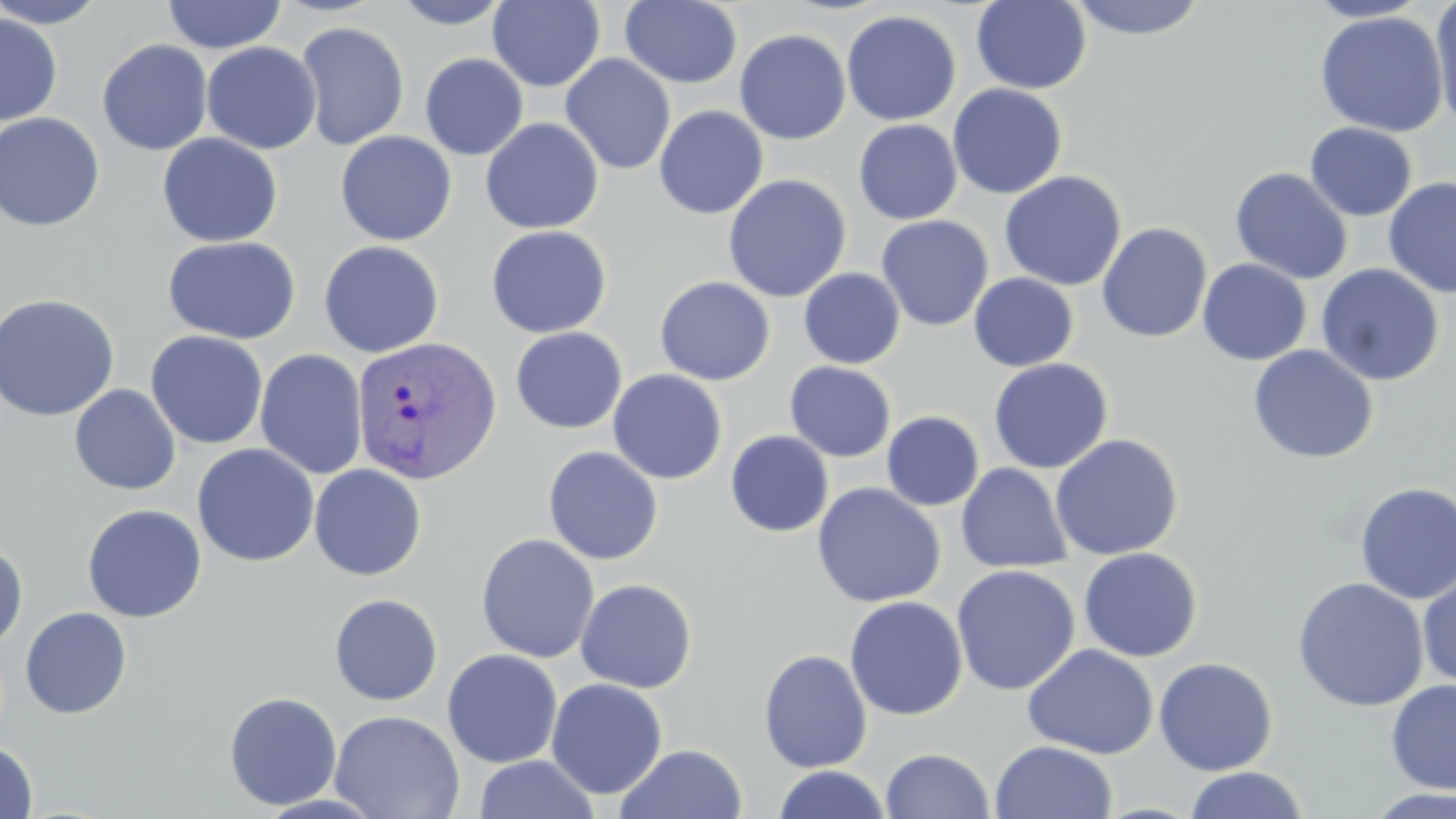

{
  "slide_level_diagnosis": "Plasmodium vivax",
  "magnification": "1000x",
  "stain": "May-Grünwald-Giemsa",
  "preparation": "thin blood smear",
  "image_size": "1456×819 pixels",
  "plasmodium_vivax_infected_red_blood_cell_locations": "approximate bounding boxes as [x1, y1, x2, y2] in pixels: [351, 334, 502, 485]",
  "field_of_view": "single",
  "uninfected_red_blood_cell_locations": "approximate bounding boxes as [x1, y1, x2, y2] in pixels: [0, 0, 111, 28], [162, 0, 287, 54], [389, 0, 515, 29], [1065, 0, 1212, 41], [1304, 0, 1433, 23], [1430, 0, 1456, 132], [488, 1, 606, 92], [619, 1, 743, 88], [971, 1, 1091, 94], [841, 10, 962, 126], [1314, 10, 1449, 137], [0, 12, 62, 127], [294, 21, 410, 151], [734, 29, 851, 145], [97, 39, 213, 155], [201, 42, 322, 154], [420, 53, 528, 160], [560, 53, 676, 175], [947, 83, 1067, 199], [653, 105, 769, 219], [0, 112, 105, 232], [480, 117, 605, 234], [854, 119, 962, 224], [1305, 122, 1417, 221], [335, 131, 457, 246], [157, 133, 283, 247], [1230, 167, 1353, 285], [999, 170, 1127, 291], [722, 174, 851, 303], [1383, 177, 1456, 298], [875, 215, 994, 331], [1097, 223, 1212, 343], [486, 225, 612, 338], [162, 235, 302, 344], [319, 240, 444, 358], [1197, 258, 1311, 366], [1315, 263, 1445, 386], [798, 268, 905, 369], [968, 273, 1079, 372], [654, 276, 775, 385], [0, 293, 120, 422], [510, 327, 627, 434], [145, 330, 268, 450], [1248, 344, 1379, 464], [255, 348, 368, 480], [988, 358, 1114, 474], [785, 361, 897, 462], [608, 369, 728, 485], [69, 384, 181, 496], [882, 411, 985, 511], [725, 430, 833, 537], [1050, 433, 1184, 561], [192, 443, 319, 567], [542, 446, 663, 565], [317, 462, 433, 703], [956, 462, 1073, 574], [309, 464, 427, 581], [1354, 481, 1456, 605], [811, 482, 946, 608], [82, 503, 207, 623], [476, 533, 599, 663], [0, 540, 28, 652], [1078, 547, 1203, 662], [951, 564, 1080, 696], [1417, 568, 1456, 689], [1292, 577, 1429, 712], [575, 578, 697, 693], [329, 594, 443, 706], [844, 596, 968, 720], [20, 607, 132, 719], [1022, 644, 1159, 759], [442, 649, 563, 768], [758, 649, 873, 773], [1153, 657, 1279, 776], [546, 678, 668, 799], [1385, 678, 1456, 795], [224, 691, 342, 810], [329, 710, 465, 819], [0, 739, 39, 818], [990, 740, 1118, 819], [615, 744, 748, 819], [880, 748, 995, 819], [473, 754, 599, 818], [771, 765, 893, 819], [1184, 766, 1309, 819], [1361, 786, 1456, 819]",
  "modality": "optical microscopy"
}